Comment on the morphology of the red blood cells.
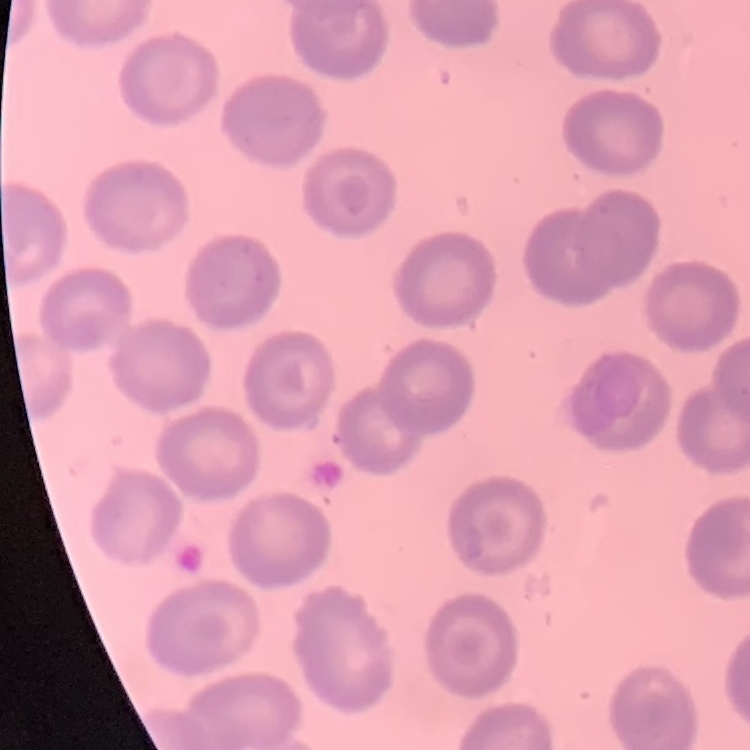
No rouleaux formation.

Summary:
  - Image type: one tile cut from a larger photomicrograph
  - Stain: Field's or Giemsa
  - Preparation: thin peripheral smear